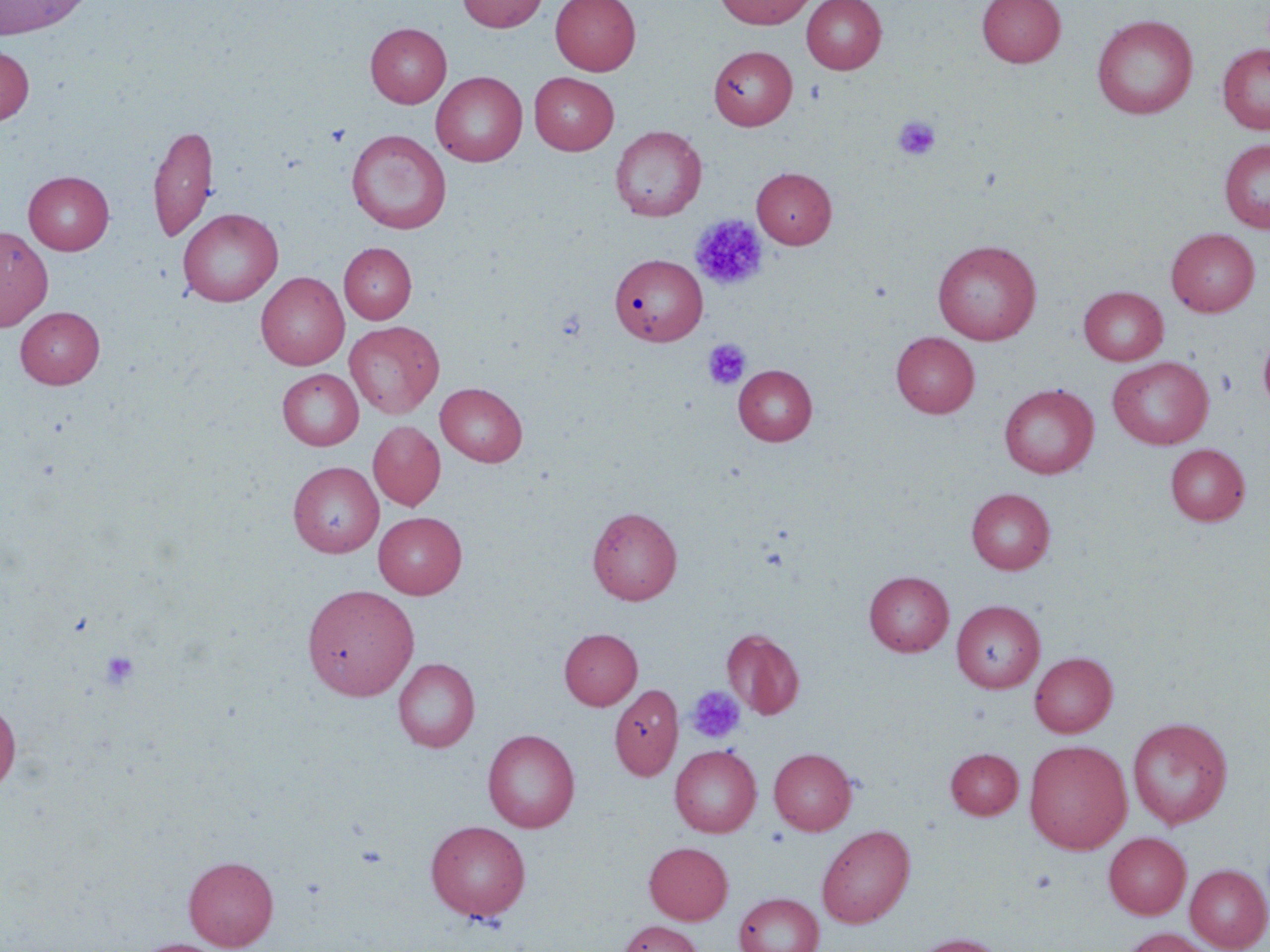

slide_level_diagnosis: negative for blood parasites
uninfected_red_blood_cell_locations: 'approximate bounding boxes as [x1, y1, x2, y2] in pixels: [0, 0, 92, 39], [457, 0, 548, 33], [551, 0, 640, 75], [714, 0, 818, 29], [802, 0, 886, 74], [977, 0, 1065, 67], [1092, 14, 1198, 119], [365, 23, 451, 108], [1217, 43, 1270, 134], [0, 44, 34, 125], [708, 46, 797, 130], [431, 71, 528, 166], [529, 72, 619, 154], [148, 122, 218, 244], [611, 126, 706, 221], [346, 130, 452, 234], [1219, 139, 1270, 233], [752, 167, 837, 248], [23, 171, 114, 255], [177, 208, 283, 306], [0, 226, 52, 330], [1166, 228, 1259, 316], [932, 240, 1041, 344], [339, 242, 416, 324], [614, 256, 709, 348], [256, 273, 349, 370], [1079, 286, 1168, 365], [15, 306, 105, 388], [344, 320, 444, 419], [1258, 331, 1270, 414], [891, 332, 979, 418], [1107, 356, 1214, 449], [734, 364, 817, 445], [278, 369, 363, 450], [436, 383, 526, 467], [999, 384, 1098, 478], [368, 421, 445, 510], [1166, 444, 1250, 525], [288, 462, 384, 557], [966, 488, 1055, 574], [587, 506, 682, 604], [373, 512, 467, 598], [864, 571, 954, 656], [302, 584, 419, 701], [952, 600, 1045, 692], [559, 628, 642, 710], [722, 629, 804, 719], [1030, 651, 1117, 737], [393, 658, 479, 752], [610, 684, 683, 779], [0, 697, 21, 795], [1127, 717, 1233, 829], [483, 729, 580, 832], [1024, 740, 1132, 854], [670, 744, 762, 837], [769, 747, 856, 835], [945, 748, 1023, 819], [426, 820, 531, 921], [817, 825, 915, 928], [1104, 832, 1191, 919], [644, 841, 733, 924], [183, 856, 279, 950], [1185, 864, 1270, 951], [734, 892, 824, 952], [617, 920, 703, 952], [1122, 927, 1217, 952], [907, 933, 1009, 952], [130, 938, 230, 952]'
stain: May-Grünwald-Giemsa
platelet_locations: 'approximate bounding boxes as [x1, y1, x2, y2] in pixels: [893, 115, 941, 160], [326, 124, 351, 147], [689, 214, 768, 291], [703, 340, 751, 390], [98, 650, 141, 691], [686, 686, 746, 744]'
modality: optical microscopy
field_of_view: single
magnification: 1000x
preparation: thin blood smear
image_size: 1270×952 pixels